Assess the background quality.
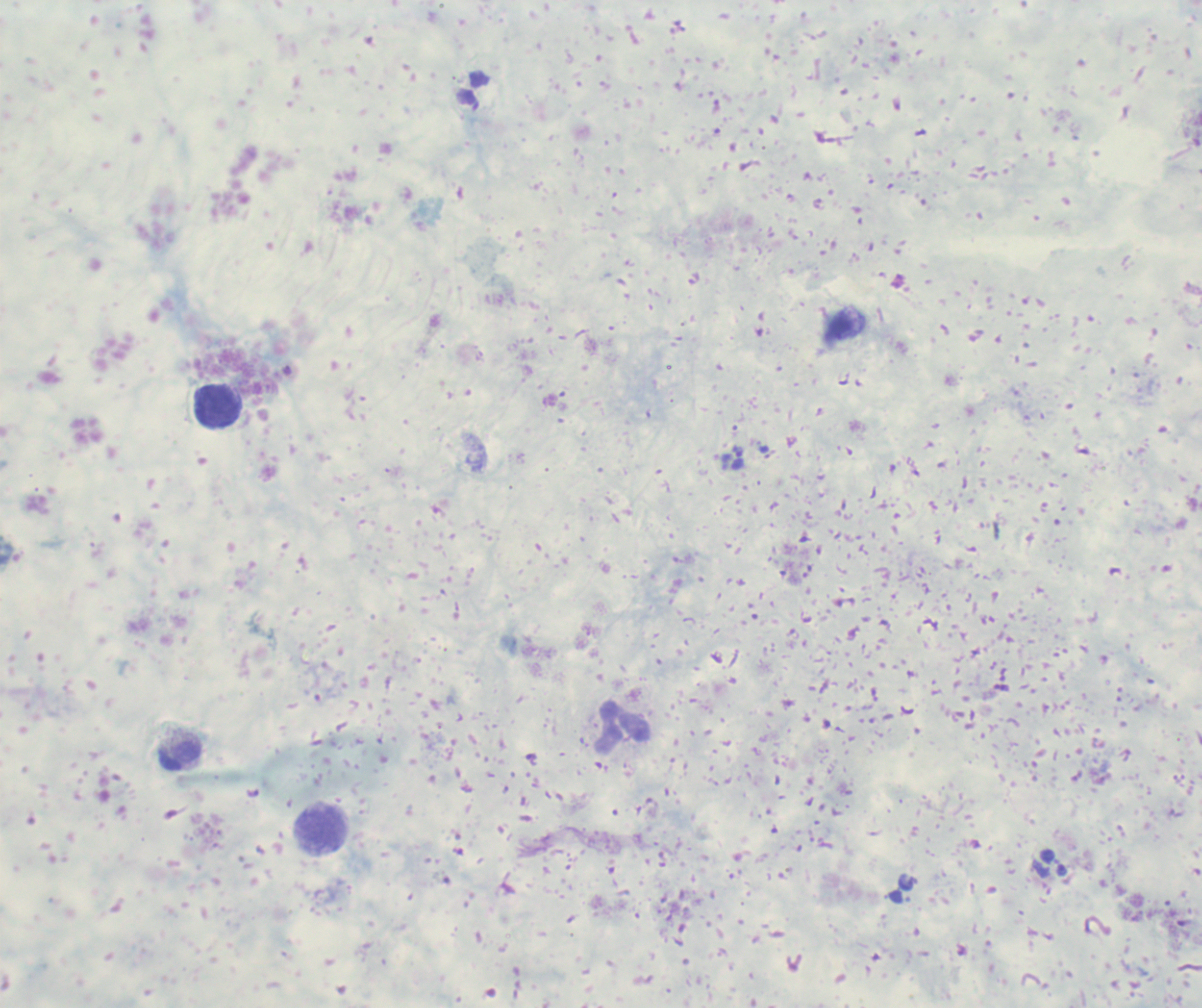

Poor.

Approximate centers as {x, y} in pixels.
Summary:
  - Trophozoite locations: {738, 457}
  - Leukocyte locations: {218, 405}, {623, 728}, {179, 754}, {322, 830}
  - Context: previously used in an actual diagnosis
  - Image size: 1202×1008 pixels
  - Preparation: thick blood film
  - Field of view: single
  - Result: malaria parasites detected
  - Stain: Romanowsky
  - Magnification: 100x